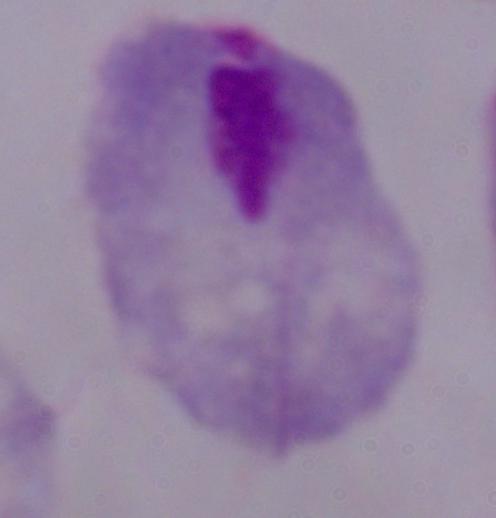
modality = micrograph
identification = trichomonad
magnification = 1000x